Identify the parasite.
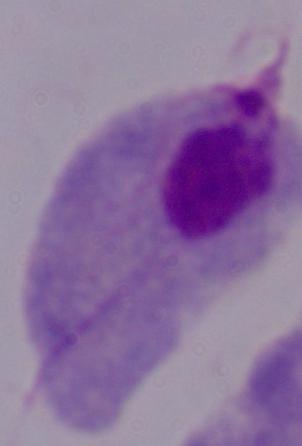
This is a trichomonad.

magnification = 1000x
modality = micrograph